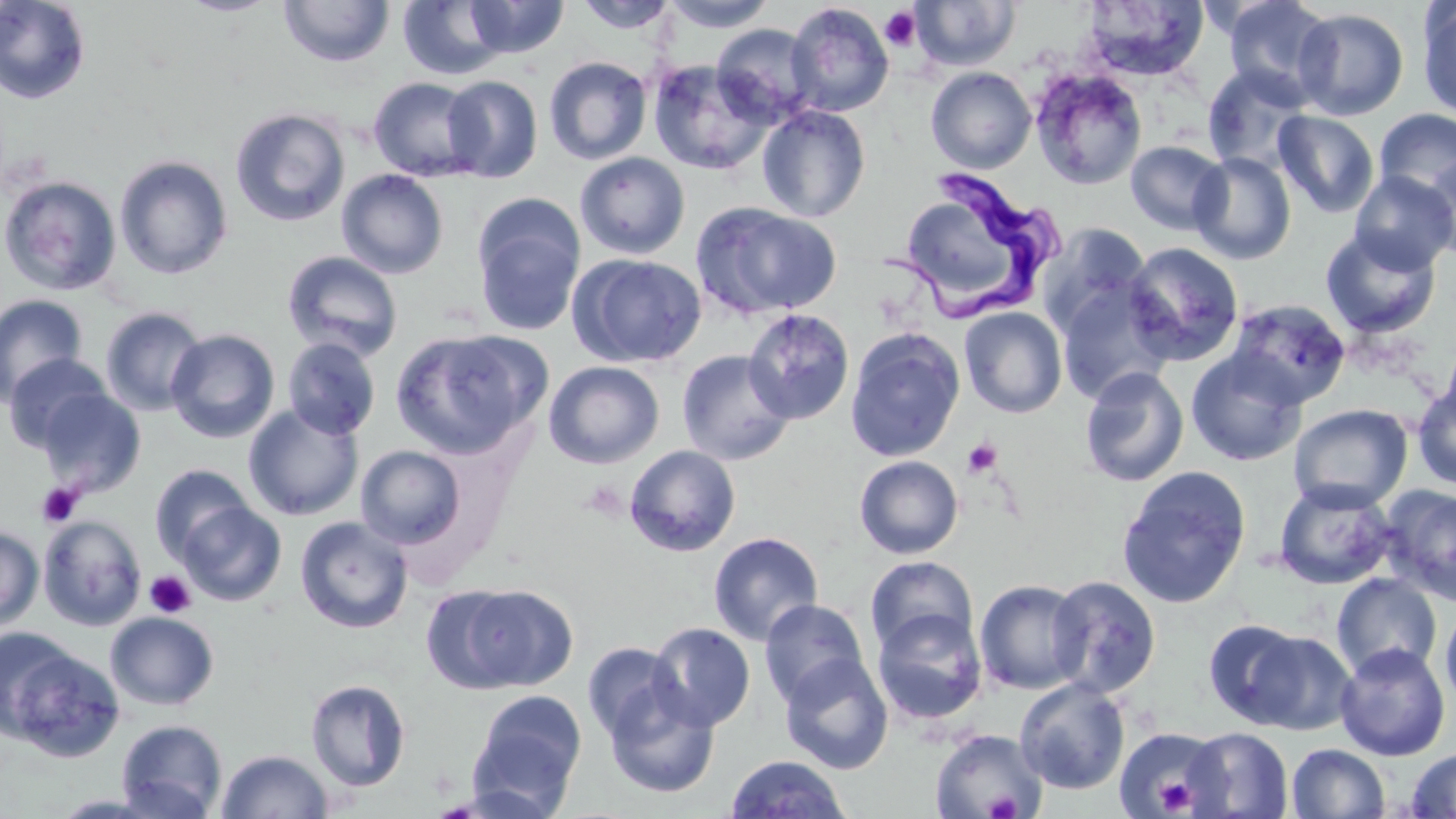

slide-level diagnosis = Trypanosoma brucei
image size = 1456×819 pixels
field of view = one of a larger specimen
modality = optical microscopy
Trypanosoma brucei locations = approximate bounding boxes as (x1,y1)-(x2,y2) corner pairs in pixels: (898,175)-(1060,341)
platelet locations = approximate bounding boxes as (x1,y1)-(x2,y2) corner pairs in pixels: (880,6)-(923,52), (962,437)-(1003,478), (36,482)-(84,528), (144,570)-(196,618), (1118,727)-(1223,819), (1154,776)-(1200,816), (984,790)-(1021,818)
magnification = 1000x
stain = May-Grünwald-Giemsa
uninfected red blood cell locations = approximate bounding boxes as (x1,y1)-(x2,y2) corner pairs in pixels: (0,0)-(92,105), (464,0)-(569,59), (660,0)-(777,32), (1220,0)-(1338,104), (175,1)-(282,17), (278,1)-(395,68), (397,1)-(511,80), (574,1)-(678,34), (911,1)-(1020,71), (1079,1)-(1210,82), (785,3)-(894,118), (1418,3)-(1456,121), (1293,8)-(1409,120), (711,23)-(821,128), (543,56)-(652,165), (647,59)-(774,175), (1201,64)-(1315,174), (926,67)-(1037,174), (1030,68)-(1148,190), (441,75)-(543,182), (368,77)-(484,181), (757,103)-(871,222), (229,107)-(351,228), (1373,107)-(1456,207), (1273,110)-(1380,218), (1125,140)-(1230,236), (1188,151)-(1296,265), (575,152)-(690,258), (1422,153)-(1456,263), (114,155)-(233,279), (337,168)-(449,279), (1349,171)-(1456,274), (0,175)-(122,296), (472,197)-(586,336), (909,200)-(1014,292), (691,202)-(842,319), (1036,223)-(1151,340), (1320,227)-(1441,339), (1121,242)-(1245,367), (281,250)-(403,362), (570,253)-(707,368), (1056,279)-(1175,404), (0,294)-(89,406), (1228,299)-(1352,408), (100,306)-(208,416), (741,307)-(855,425), (959,307)-(1068,418), (390,327)-(548,458), (845,328)-(965,462), (166,329)-(280,443), (281,337)-(382,440), (1440,337)-(1456,430), (676,349)-(796,466), (1186,349)-(1307,466), (3,353)-(113,453), (543,361)-(665,469), (1079,366)-(1189,487), (1412,384)-(1456,490), (35,387)-(146,496), (1288,403)-(1413,512), (243,404)-(364,521), (355,444)-(468,549), (624,444)-(741,557), (854,455)-(963,559), (149,464)-(255,563), (1116,466)-(1252,608), (1273,480)-(1398,590), (1381,483)-(1456,607), (177,500)-(287,607), (37,514)-(147,631), (294,516)-(413,634), (0,526)-(45,634), (708,531)-(824,646), (865,555)-(978,658), (1331,572)-(1442,680), (1047,576)-(1162,697), (974,579)-(1089,694), (428,580)-(579,695), (759,599)-(870,707), (1440,605)-(1456,709), (872,608)-(988,725), (105,612)-(219,710), (1203,618)-(1310,729), (647,622)-(756,732), (1,628)-(78,735), (1242,629)-(1358,736), (2,641)-(125,762), (583,642)-(686,745), (1335,643)-(1450,761), (778,653)-(894,775), (305,678)-(412,793), (1014,678)-(1130,795), (603,682)-(720,799), (468,690)-(587,810), (116,718)-(227,819), (1184,727)-(1293,818), (1114,728)-(1225,819), (929,729)-(1048,819), (1287,744)-(1390,819), (1405,747)-(1456,818), (217,749)-(333,818), (725,754)-(852,818)
preparation = thin blood smear